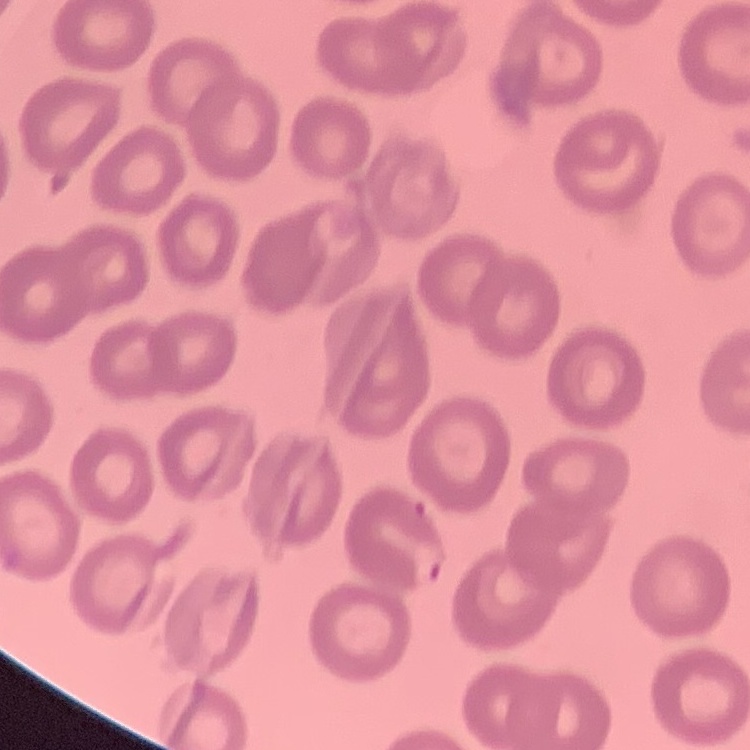

The erythrocytes show no rouleaux formation. Field's or Giemsa stain. Square crop of a larger photomicrograph. Thin peripheral smear.